State which cell type is depicted.
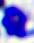
This is a leukocyte.

modality: micrograph
magnification: 400x